Describe the morphology of the red blood cells.
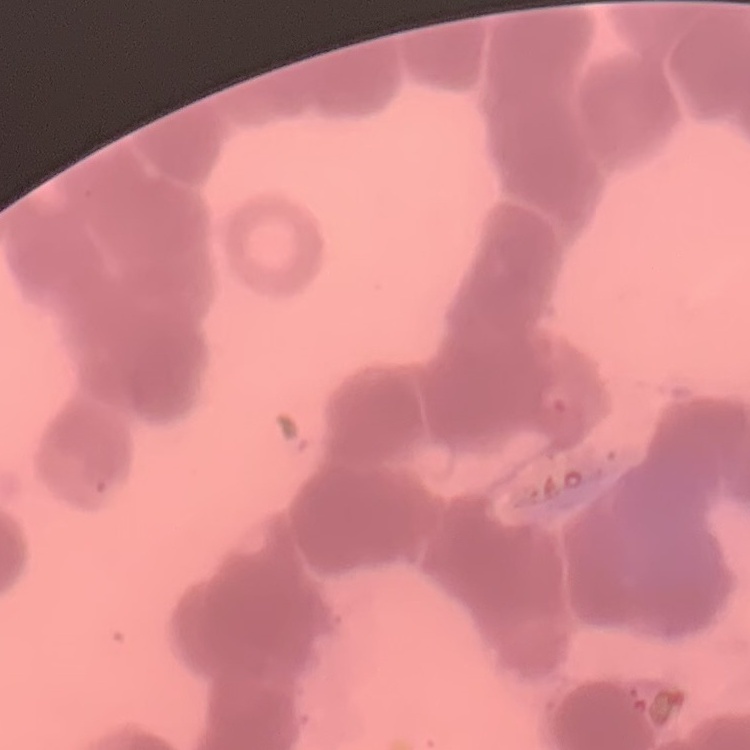

Rouleaux formation.

One tile cut from a larger photomicrograph. Stained with either Field's or Giemsa. Thin peripheral smear.